Locate and identify every blood parasite.
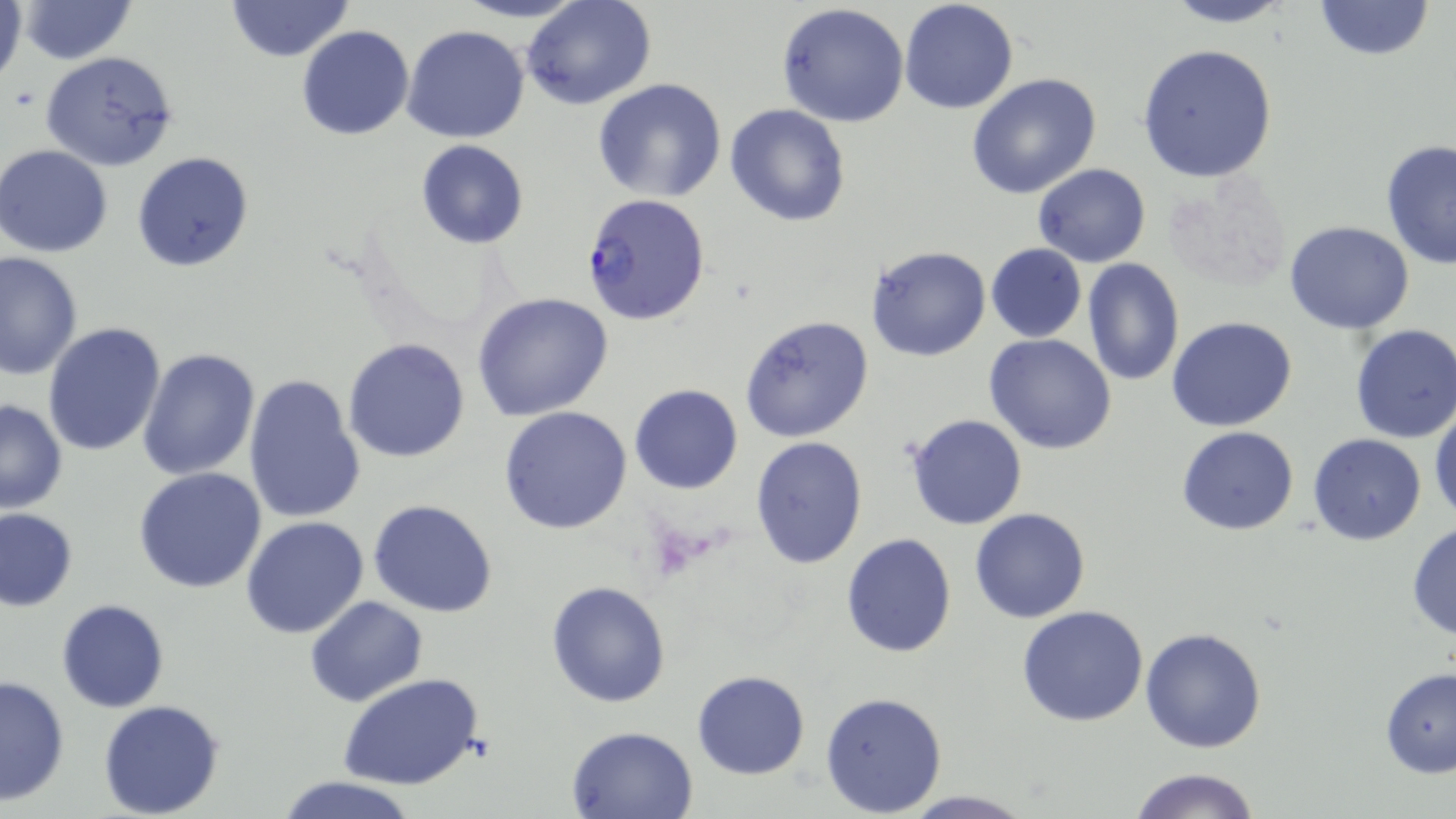
Approximate bounding boxes as (x1, y1, x2, y2) in pixels.
Plasmodium falciparum-infected red blood cells: (581, 194, 711, 323).
No Plasmodium ovale, Plasmodium malariae, Plasmodium vivax, Babesia divergens, or Trypanosoma brucei observed.

slide-level diagnosis = Plasmodium falciparum
preparation = thin blood smear
uninfected red blood cell locations = approximate bounding boxes as (x1, y1, x2, y2) in pixels: (18, 0, 137, 64), (225, 0, 354, 62), (451, 0, 593, 24), (521, 0, 657, 111), (900, 0, 1018, 114), (1159, 0, 1300, 27), (1310, 0, 1436, 61), (0, 2, 28, 91), (777, 3, 909, 128), (297, 25, 415, 142), (403, 25, 531, 145), (1138, 44, 1278, 182), (40, 51, 181, 172), (967, 73, 1100, 198), (592, 78, 727, 204), (724, 103, 852, 227), (1380, 139, 1456, 271), (415, 140, 528, 250), (1, 144, 116, 257), (131, 151, 256, 273), (1032, 163, 1150, 266), (1166, 170, 1291, 293), (1284, 221, 1415, 334), (985, 244, 1087, 342), (868, 246, 991, 361), (0, 251, 83, 381), (1081, 259, 1184, 387), (471, 292, 615, 421), (739, 315, 875, 443), (1166, 316, 1297, 433), (42, 321, 167, 455), (1349, 323, 1456, 445), (983, 334, 1117, 456), (343, 338, 471, 463), (136, 347, 262, 481), (244, 374, 365, 523), (628, 383, 742, 495), (0, 399, 69, 515), (1430, 403, 1455, 523), (500, 405, 633, 535), (904, 414, 1029, 531), (1176, 424, 1300, 537), (1308, 433, 1427, 545), (749, 436, 869, 571), (135, 466, 268, 593), (368, 499, 498, 619), (970, 506, 1091, 623), (0, 507, 78, 611), (241, 517, 370, 639), (1406, 521, 1456, 639), (841, 532, 957, 659), (546, 579, 671, 707), (306, 595, 429, 707), (57, 600, 170, 713), (1016, 606, 1149, 727), (1140, 627, 1268, 753), (1379, 667, 1456, 777), (691, 670, 811, 780), (337, 673, 486, 791), (0, 674, 71, 806), (820, 690, 948, 815), (99, 701, 226, 818), (567, 724, 698, 818), (1126, 767, 1262, 819), (276, 775, 420, 819), (897, 790, 1038, 818)
stain = May-Grünwald-Giemsa
field of view = single
modality = optical microscopy
image size = 1456×819 pixels
magnification = 1000x